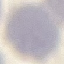

Summary:
  - Malaria status: uninfected
  - Stain: Giemsa
  - Image type: automatically extracted cell patch, resized to 64 × 64 pixels
  - Capture: smartphone through the microscope eyepiece
  - Preparation: thin blood smear